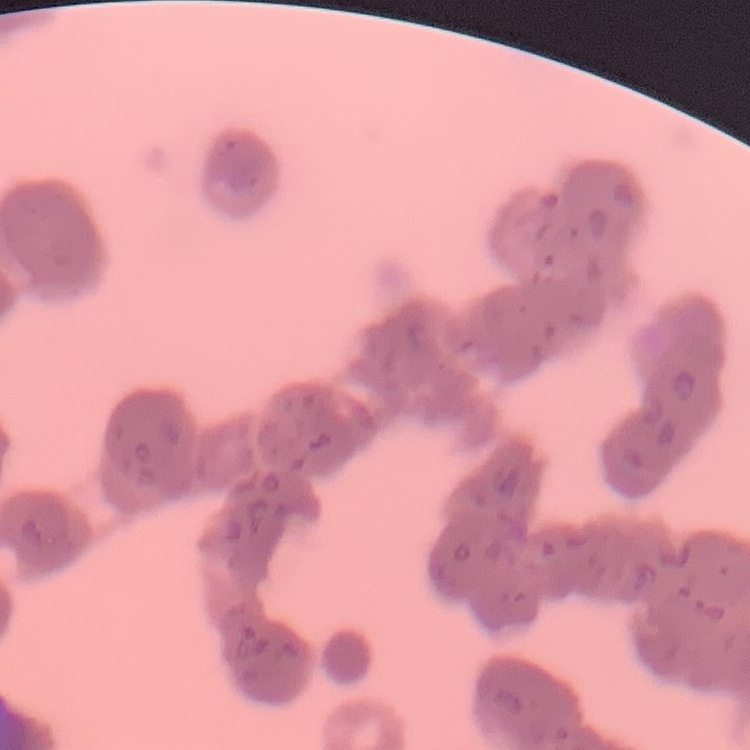 The erythrocytes exhibit rouleaux formation. Square crop of a larger photomicrograph. Thin blood film. Stained with either Field's or Giemsa.